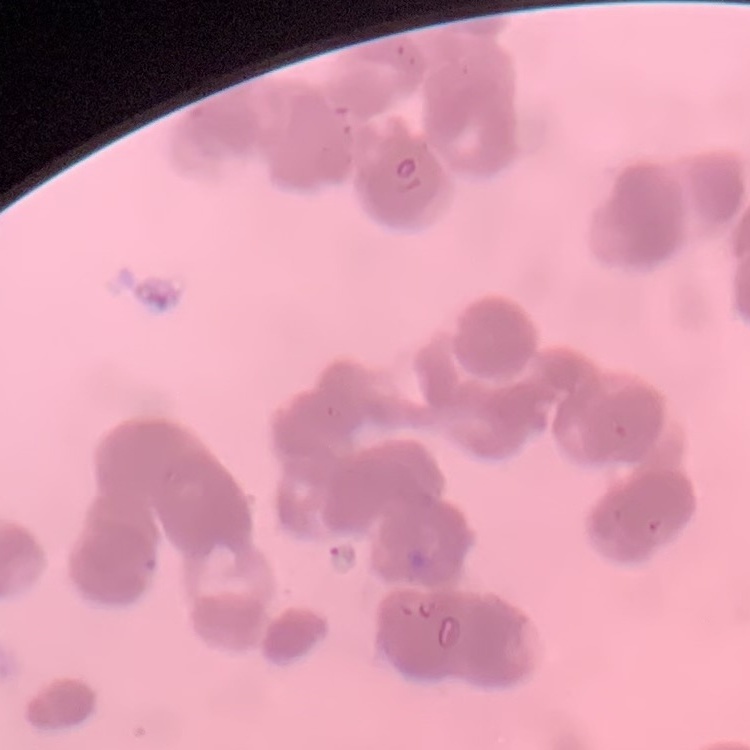

The erythrocytes exhibit rouleaux formation. Field's or Giemsa stain. One tile cut from a larger photomicrograph. Thin blood film.